Identify the parasite.
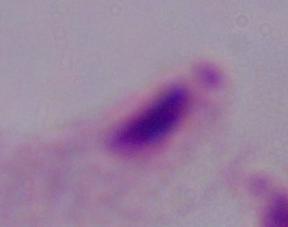

This is a trichomonad.

magnification = 1000x
modality = micrograph